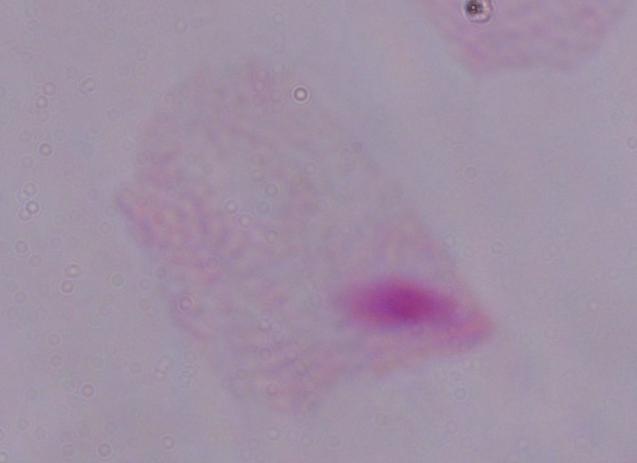

Micrograph. A trichomonad is shown. 1000x magnification.